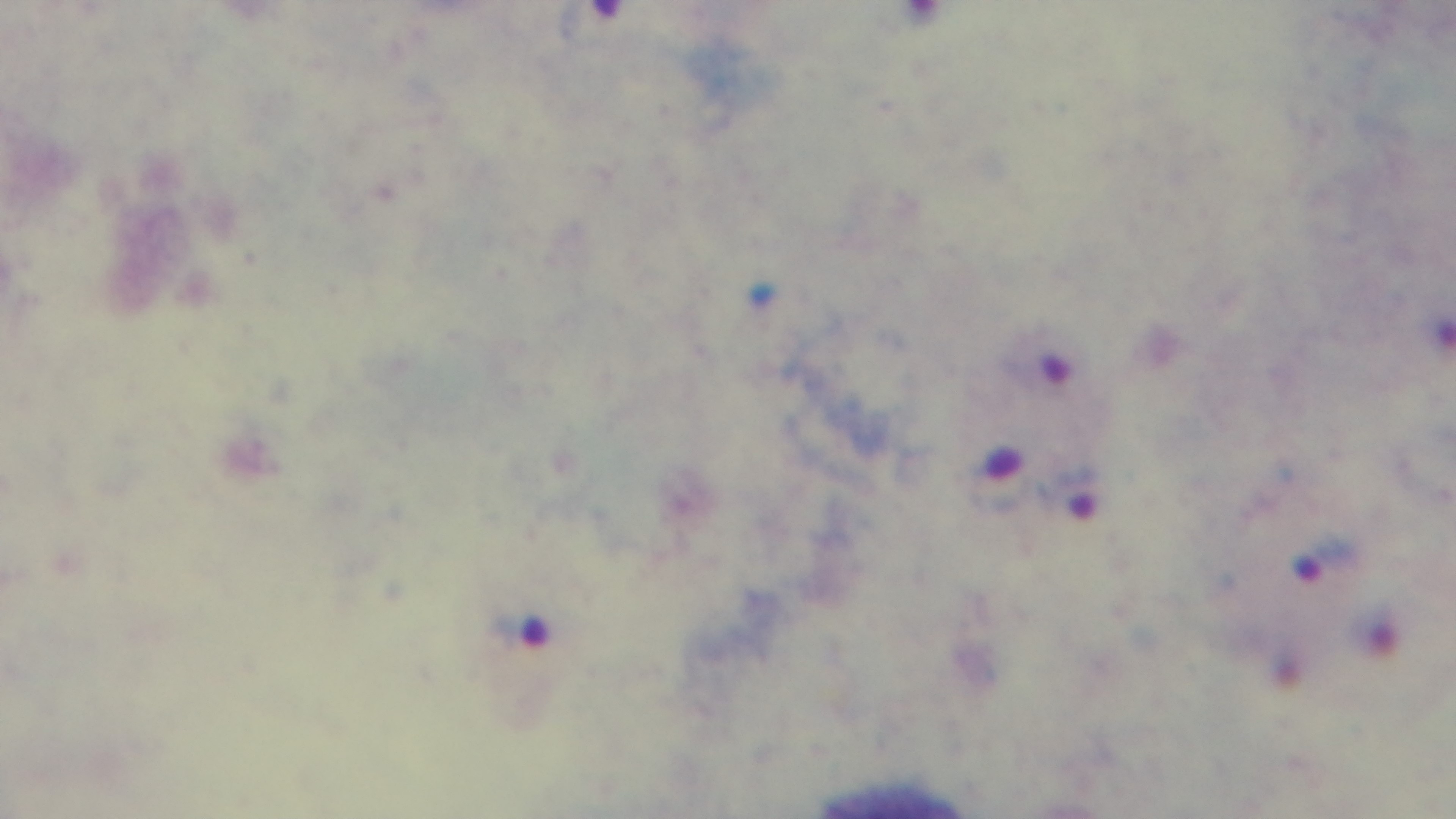

Captured with a mounted 4K digital camera. Malaria status: positive. Giemsa-stained. Light microscopy. One field from the slide. Preparation: thick blood film. 100x oil-immersion objective.